State which parasite is depicted.
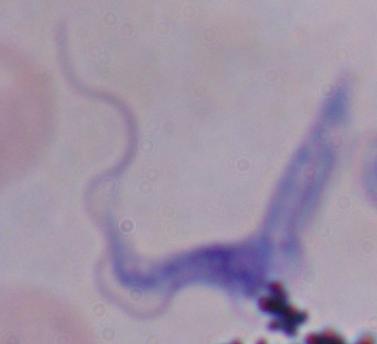

A trypanosome.

{
  "modality": "photomicrograph",
  "magnification": "1000x"
}